Assess this cell for malaria.
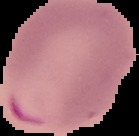

Parasitized.

image size = 139×136 pixels
preparation = thin blood smear
image type = segmented cell region on a black background